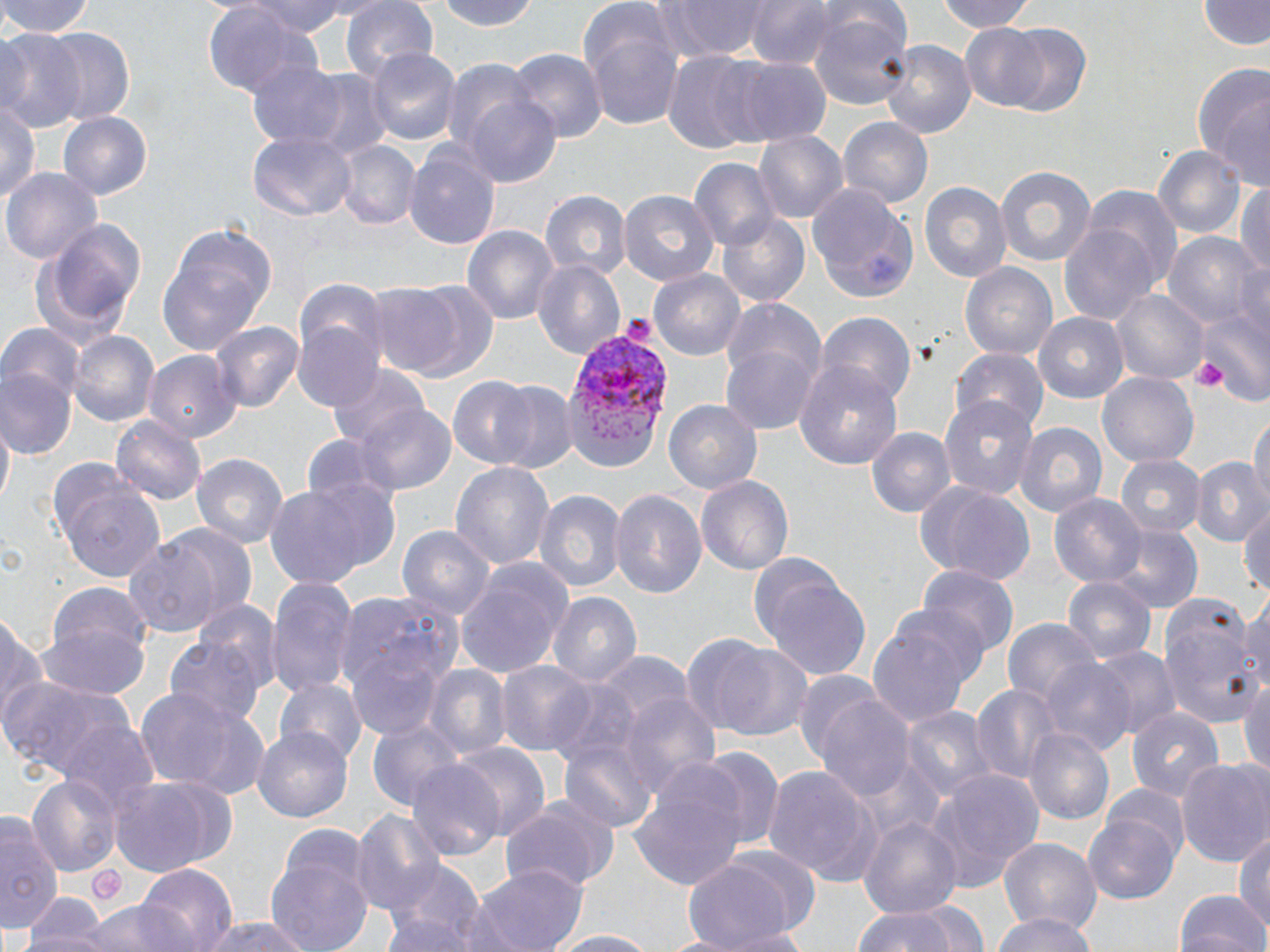

{
  "slide_level_diagnosis": "Plasmodium vivax",
  "modality": "optical microscopy",
  "uninfected_red_blood_cell_locations": "approximate bounding boxes as (x1,y1)-(x2,y2) corner pairs in pixels: (0,0)-(97,38), (244,0)-(353,37), (435,0)-(541,32), (661,0)-(770,60), (743,0)-(832,69), (930,0)-(1041,33), (342,1)-(437,84), (1203,1)-(1268,52), (202,5)-(318,102), (579,9)-(688,132), (807,9)-(916,113), (999,23)-(1094,118), (961,27)-(1054,111), (0,29)-(85,135), (39,29)-(137,126), (880,38)-(975,141), (363,47)-(463,147), (509,50)-(607,144), (660,54)-(767,151), (246,57)-(349,151), (716,58)-(831,145), (1190,65)-(1270,185), (301,71)-(390,160), (461,92)-(562,188), (0,97)-(41,209), (59,112)-(152,199), (837,116)-(934,212), (755,130)-(848,222), (249,134)-(353,219), (333,141)-(418,231), (1152,142)-(1245,240), (404,145)-(501,252), (689,156)-(778,251), (992,164)-(1096,268), (5,166)-(102,264), (918,179)-(1012,287), (1235,179)-(1270,281), (807,181)-(920,303), (1087,187)-(1182,289), (542,190)-(629,283), (618,190)-(719,288), (718,213)-(813,308), (27,215)-(149,349), (1059,222)-(1160,326), (462,225)-(558,328), (155,227)-(276,359), (1165,231)-(1263,332), (532,260)-(625,361), (960,261)-(1058,362), (648,267)-(746,362), (371,279)-(495,382), (295,280)-(385,370), (1111,292)-(1207,383), (721,297)-(826,398), (1197,309)-(1270,410), (1037,312)-(1130,405), (819,315)-(915,410), (210,320)-(303,412), (1,324)-(86,405), (292,324)-(386,413), (70,329)-(159,427), (721,341)-(819,435), (952,347)-(1048,434), (144,351)-(240,441), (793,360)-(903,472), (325,362)-(427,448), (1097,371)-(1199,470), (1,372)-(74,459), (450,378)-(540,469), (491,383)-(576,475), (938,395)-(1039,499), (663,399)-(763,494), (352,403)-(456,496), (112,415)-(206,504), (1247,416)-(1269,511), (1,420)-(14,514), (1017,421)-(1107,519), (865,426)-(954,517), (194,452)-(288,550), (1115,455)-(1202,541), (1190,455)-(1270,552), (451,461)-(555,576), (49,465)-(168,582), (695,475)-(793,576), (916,479)-(1036,585), (260,480)-(384,591), (610,486)-(708,600), (533,487)-(625,592), (1050,493)-(1147,587), (1239,501)-(1270,603), (164,523)-(257,615), (396,523)-(499,626), (1107,526)-(1203,613), (124,537)-(222,638), (751,560)-(873,679), (453,562)-(571,678), (917,566)-(1016,664), (1062,576)-(1153,667), (266,577)-(356,699), (44,582)-(154,664), (337,591)-(466,716), (546,591)-(643,690), (1157,592)-(1261,730), (1239,593)-(1270,697), (0,611)-(46,735), (867,614)-(978,730), (1003,617)-(1102,712), (37,619)-(152,700), (166,636)-(265,731), (702,639)-(816,741), (1091,645)-(1180,741), (596,655)-(692,730), (1040,660)-(1136,755), (498,662)-(596,757), (423,664)-(512,762), (1241,670)-(1270,777), (2,675)-(133,783), (276,676)-(365,766), (546,678)-(644,774), (973,683)-(1062,787), (132,685)-(258,793), (617,689)-(721,798), (814,692)-(915,803), (899,705)-(991,804), (1128,707)-(1223,803), (367,717)-(462,810), (54,721)-(157,817), (1025,726)-(1116,828), (251,728)-(351,821), (559,733)-(656,834), (452,743)-(549,842), (696,745)-(784,853), (1176,757)-(1270,869), (406,758)-(504,859), (854,759)-(944,844), (762,765)-(875,884), (928,768)-(1043,889), (628,771)-(749,892), (27,773)-(122,878), (108,776)-(234,874), (1105,784)-(1191,862), (503,795)-(618,893), (352,810)-(447,916), (859,812)-(963,924), (0,813)-(60,931), (1086,815)-(1182,902), (1232,828)-(1270,931), (268,834)-(374,952), (1001,838)-(1100,935), (679,859)-(797,952), (134,861)-(238,951), (383,862)-(487,951), (473,865)-(586,952), (1175,888)-(1266,952), (78,899)-(199,952), (916,899)-(988,951), (24,900)-(107,952), (852,902)-(967,952), (987,912)-(1103,952), (202,916)-(318,952), (715,926)-(823,951), (548,929)-(658,952)",
  "magnification": "1000x",
  "stain": "May-Grünwald-Giemsa",
  "preparation": "thin blood film",
  "platelet_locations": "approximate bounding boxes as (x1,y1)-(x2,y2) corner pairs in pixels: (625,313)-(653,340), (1193,360)-(1227,392), (88,864)-(126,906)",
  "field_of_view": "single",
  "image_size": "1270×952 pixels",
  "plasmodium_vivax_infected_red_blood_cell_locations": "approximate bounding boxes as (x1,y1)-(x2,y2) corner pairs in pixels: (559,329)-(671,446)"
}